Describe the morphology of the red blood cells.
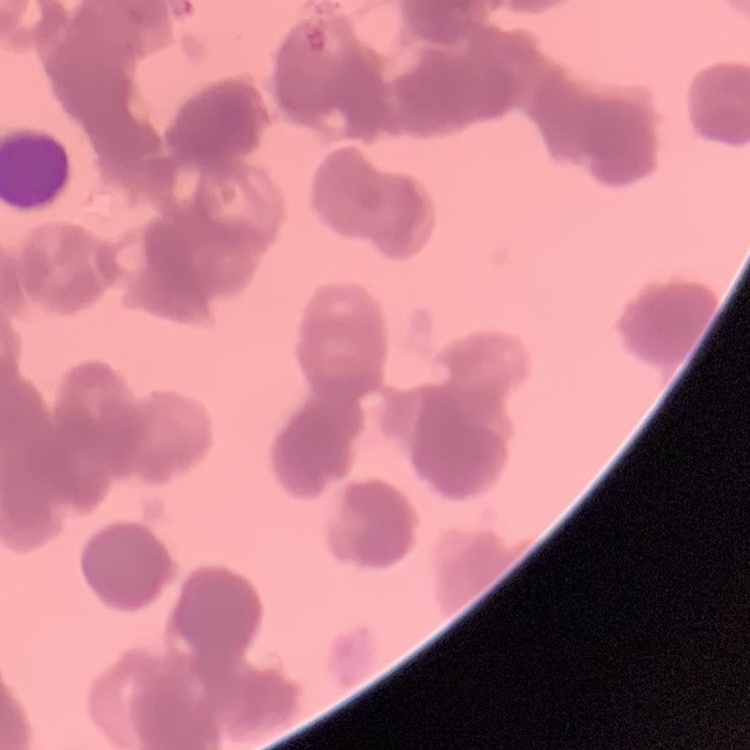
Rouleaux formation.

Summary:
  - Stain: Field's or Giemsa
  - Preparation: thin peripheral smear
  - Image type: square crop of a larger photomicrograph